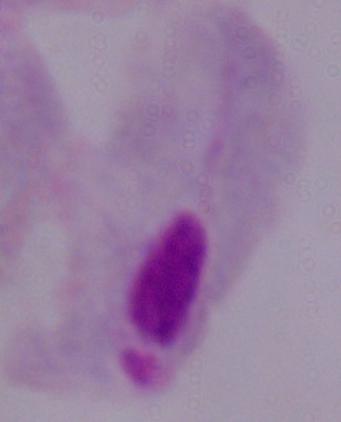 A trichomonad is shown. Micrograph. 1000x magnification.